Classify this cell by malaria status.
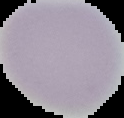

Uninfected.

Summary:
  - Image type: segmented cell region on a black background
  - Image size: 124×118 pixels
  - Preparation: thin blood film